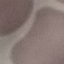 Malaria status: uninfected. Acquired by smartphone through the microscope eyepiece. Thin blood smear. Automatically extracted cell patch, resized to 64 × 64 pixels. Giemsa stain.